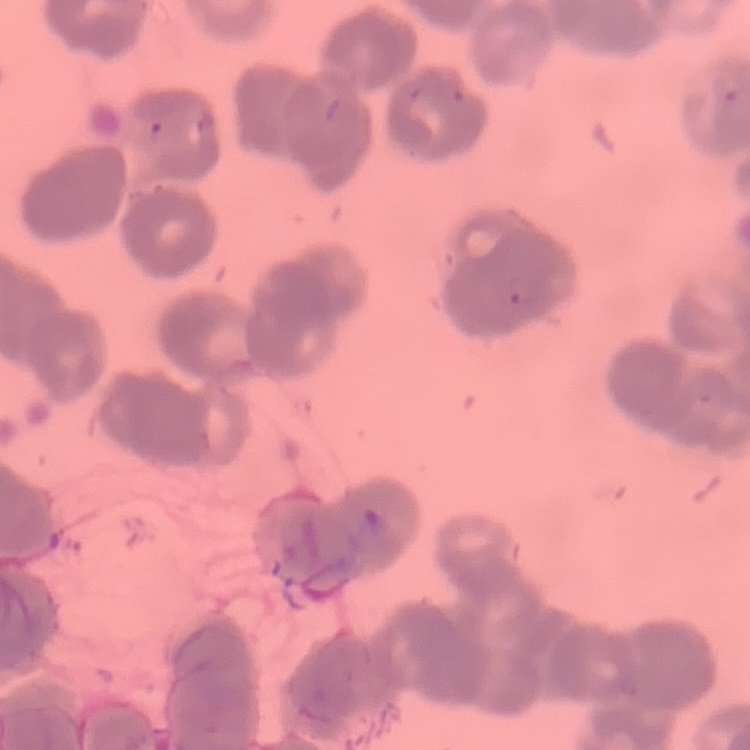
Summary:
  - Erythrocyte morphology: rouleaux formation
  - Stain: Field's or Giemsa
  - Image type: one tile cut from a larger photomicrograph
  - Preparation: thin blood film